Identify the parasite.
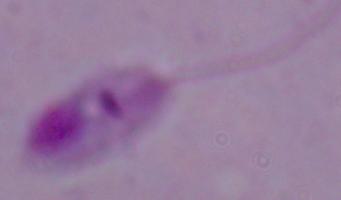
This is Leishmania.

Summary:
  - Modality: photomicrograph
  - Magnification: 1000x